State the preparation type.
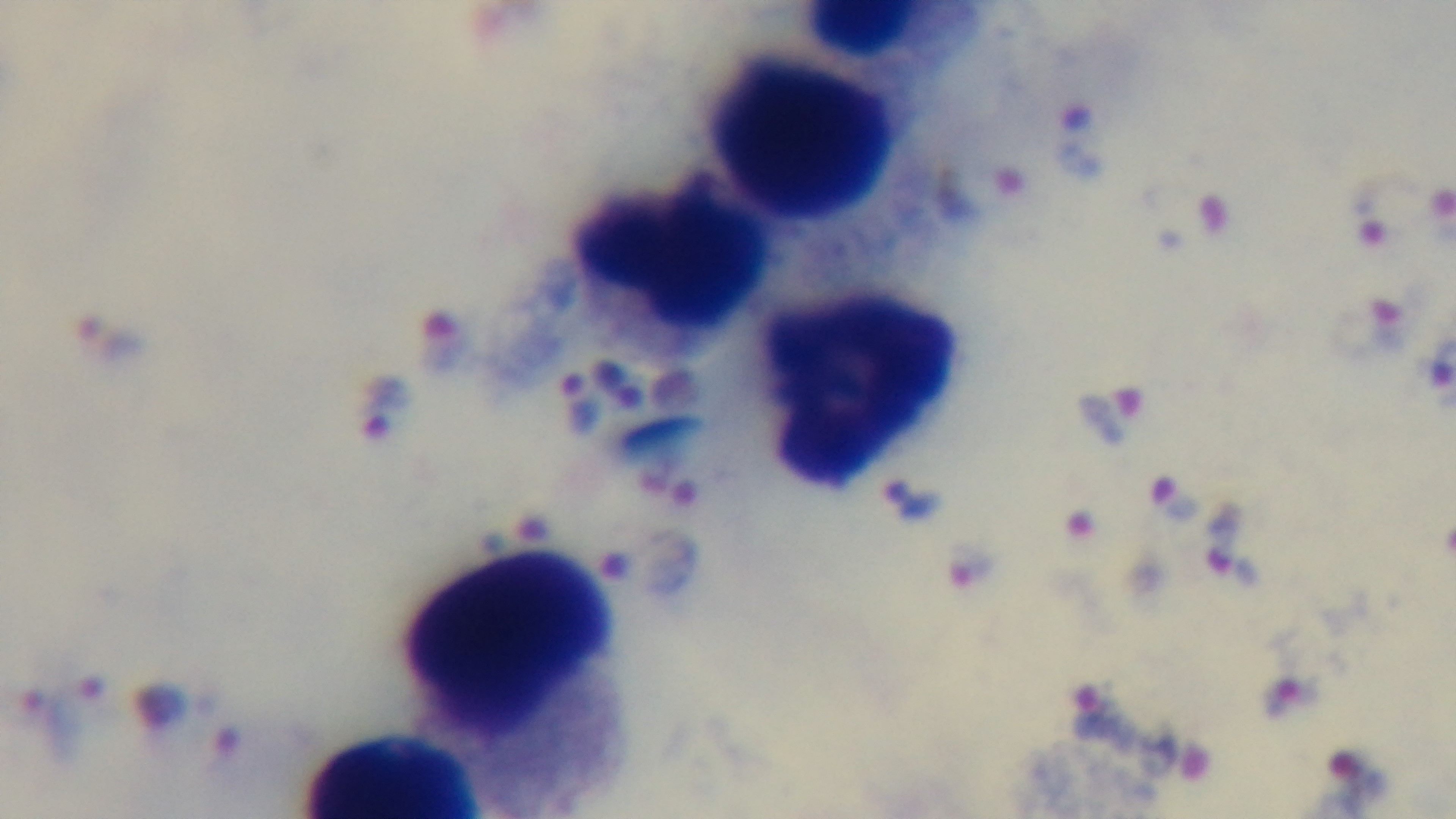

It is a thick blood film.

capture: mounted 4K digital camera
malaria_status: positive
stain: Giemsa
modality: light microscopy
field_of_view: single
objective: 100x oil immersion